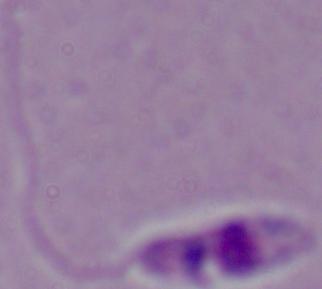 A Leishmania parasite is shown. Photomicrograph. 1000x magnification.